Report the malaria status of this cell.
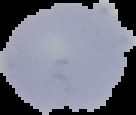

Uninfected.

Cell region segmented out of the field of view; the surrounding area is masked to black. Image is 136×115 pixels. From a thin blood film.